Assess this cell for malaria.
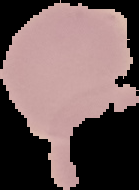
Uninfected.

image size = 139×190 pixels
image type = cell region segmented out of the field of view; surrounding area masked to black
preparation = thin blood film